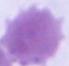

Micrograph. Captured at 1000x magnification. A red blood cell is shown.